Identify the cell.
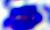
A leukocyte.

Photomicrograph. 400x magnification.